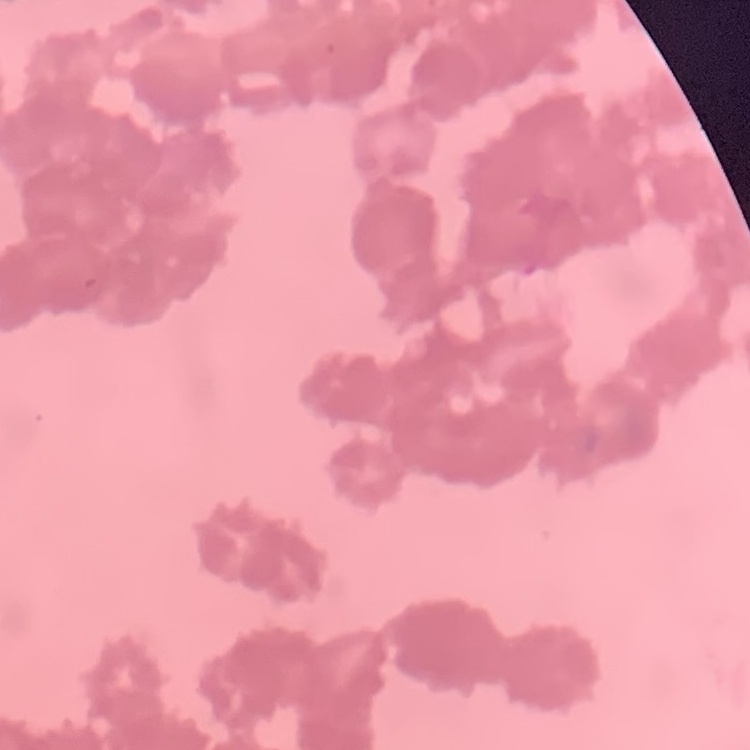
erythrocyte morphology = rouleaux formation
preparation = thin blood smear
image type = one tile cut from a larger photomicrograph
stain = Field's or Giemsa